State which malaria species this is.
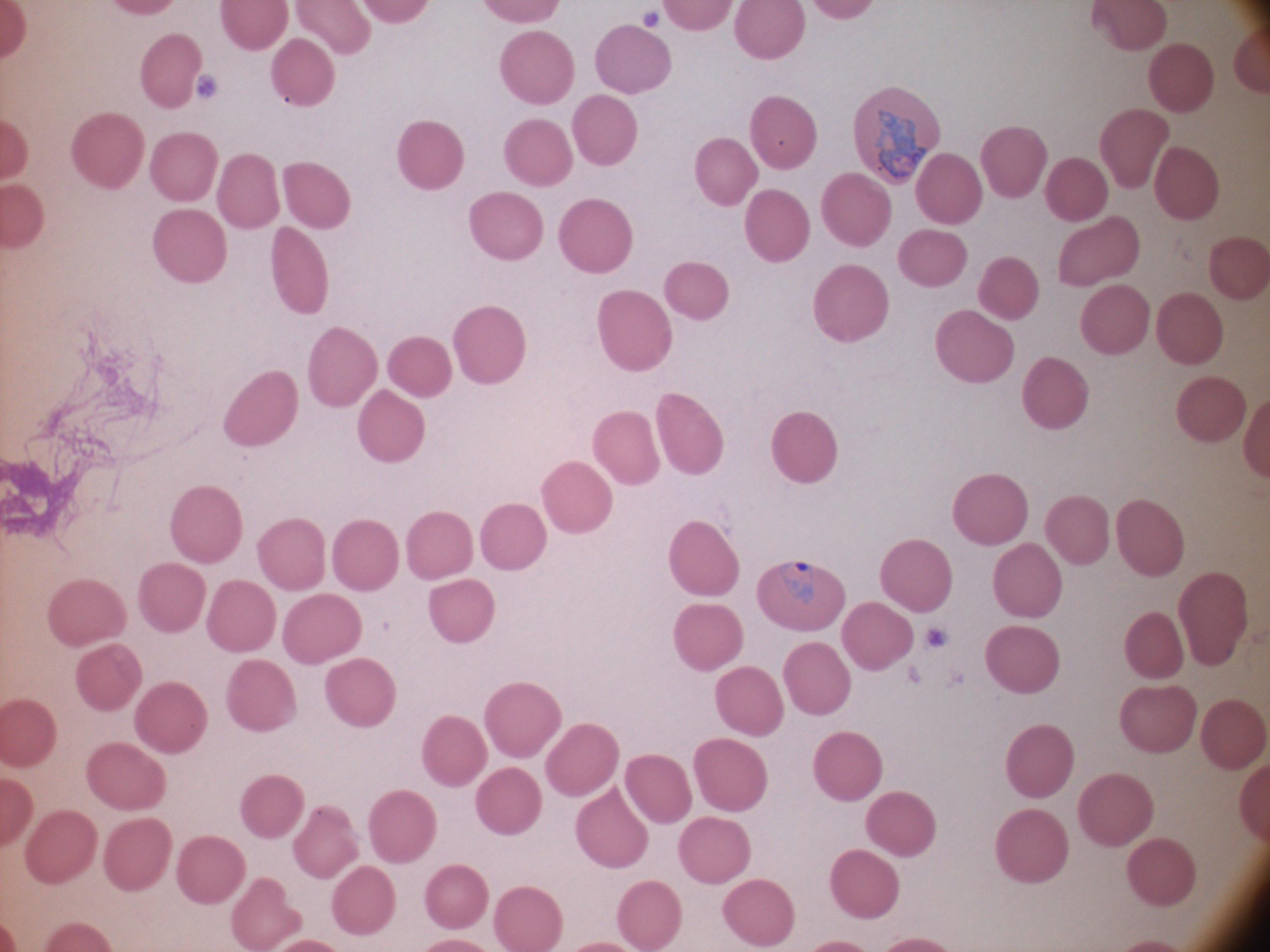

Plasmodium ovale.

Approximate bounding boxes as [x1, y1, x2, y2] in pixels, from the source annotation, which is not necessarily exhaustive.
Summary:
  - Malaria parasite locations: [779, 561, 814, 604]
  - Magnification: 100x
  - Preparation: thin blood film
  - Field of view: one from this slide
  - Stain: Giemsa
  - Image size: 1270×952 pixels
  - Microscope: Leica DM2000 with built-in camera